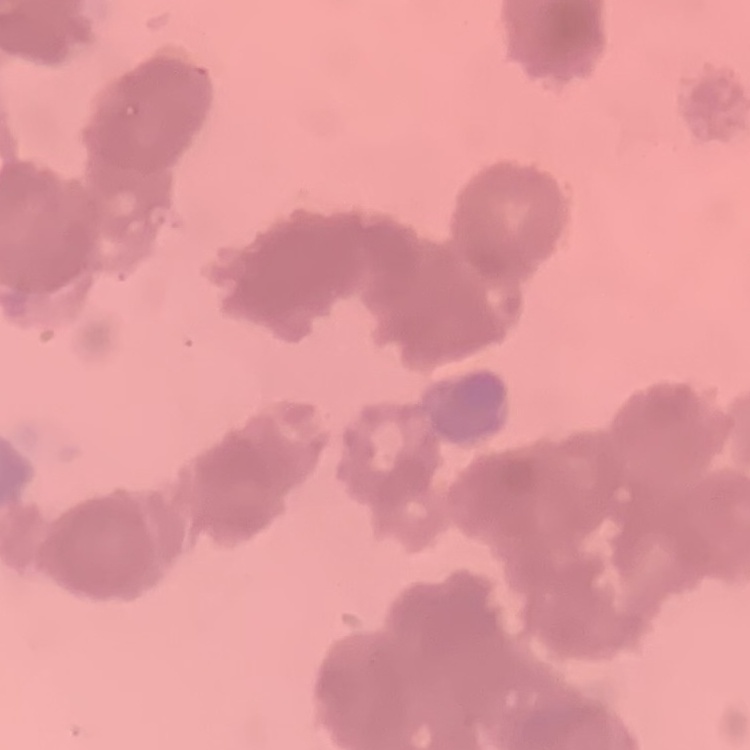
erythrocyte morphology = rouleaux formation
stain = Field's or Giemsa
image type = square crop of a larger photomicrograph
preparation = thin blood smear